Report the malaria status of this cell.
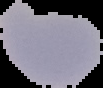

It is parasitized.

image_type: cell region segmented out of the field of view; surrounding area masked to black
preparation: thin blood film
image_size: 103×88 pixels